Report the malaria status of this cell.
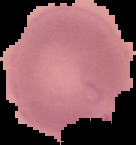
It is parasitized.

Summary:
  - Image size: 136×145 pixels
  - Image type: segmented cell region on a black background
  - Preparation: thin blood film